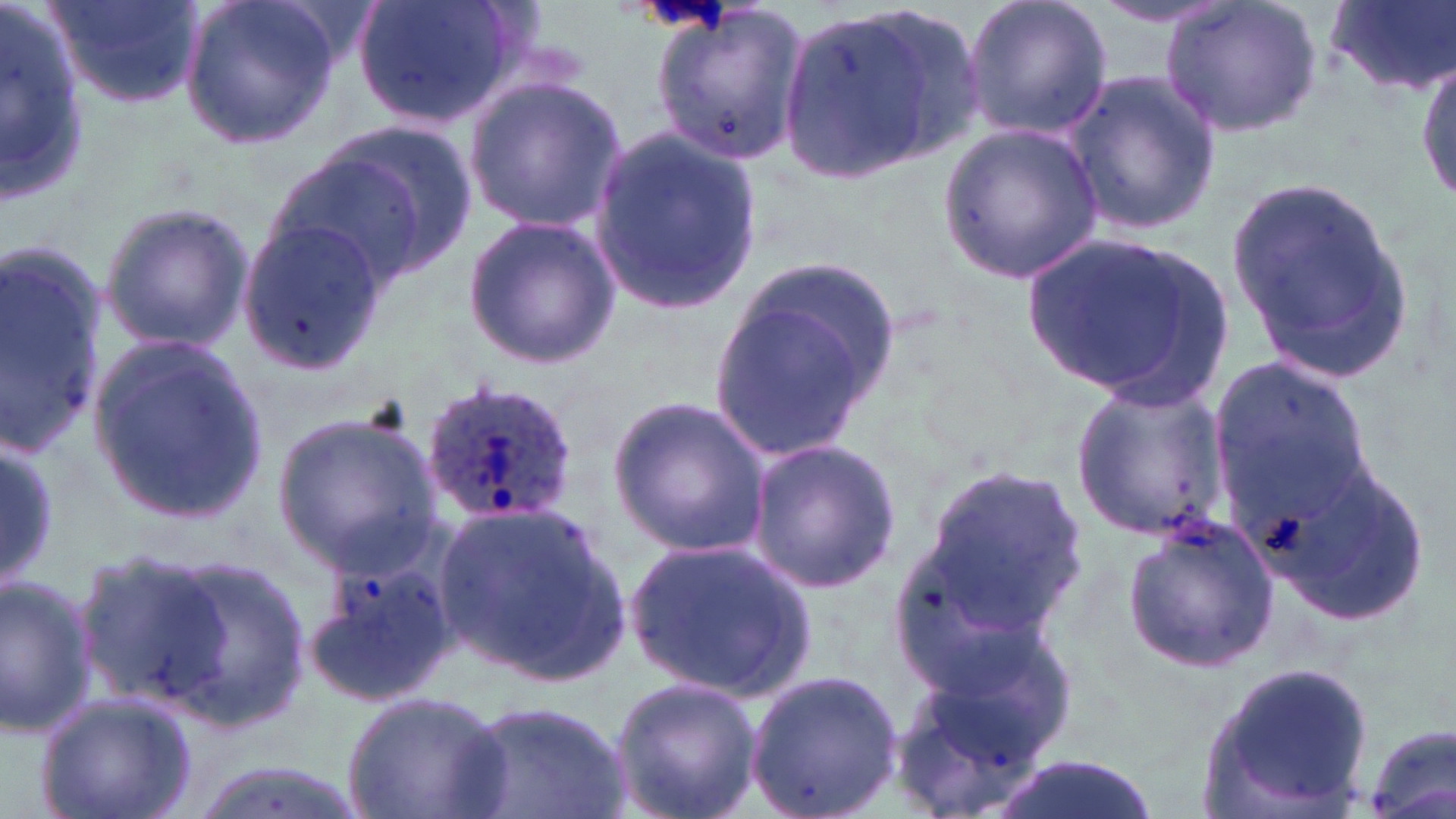
slide_level_diagnosis: Plasmodium ovale
magnification: 1000x
plasmodium_ovale_infected_red_blood_cell_locations: 'approximate bounding boxes as (x1, y1, x2, y2) in pixels: (420, 375, 582, 527)'
uninfected_red_blood_cell_locations: 'approximate bounding boxes as (x1, y1, x2, y2) in pixels: (0, 0, 96, 213), (48, 0, 206, 108), (178, 0, 342, 153), (352, 0, 523, 131), (961, 0, 1112, 142), (1159, 0, 1323, 139), (1322, 0, 1456, 97), (647, 1, 811, 163), (1089, 1, 1238, 27), (774, 14, 927, 185), (1415, 51, 1455, 213), (1059, 67, 1220, 237), (462, 75, 628, 233), (940, 123, 1103, 284), (271, 126, 476, 290), (589, 128, 765, 313), (1229, 177, 1418, 385), (97, 200, 254, 354), (461, 214, 621, 369), (236, 215, 392, 374), (1017, 231, 1233, 406), (0, 240, 111, 457), (702, 260, 900, 466), (84, 329, 265, 525), (1209, 353, 1374, 526), (1068, 380, 1230, 540), (609, 395, 771, 562), (271, 410, 443, 570), (744, 438, 902, 593), (0, 443, 60, 588), (1259, 458, 1429, 629), (917, 465, 1088, 637), (433, 500, 629, 683), (1119, 517, 1280, 677), (622, 536, 815, 699), (888, 546, 1049, 704), (69, 548, 247, 715), (304, 556, 456, 710), (143, 557, 311, 726), (0, 573, 98, 738), (884, 648, 1073, 816), (1194, 663, 1379, 819), (744, 671, 904, 818), (606, 675, 761, 819), (339, 688, 514, 819), (35, 690, 199, 819), (460, 698, 632, 819), (1360, 725, 1456, 819), (987, 754, 1160, 819), (182, 759, 369, 819)'
image_size: 1456×819 pixels
modality: optical microscopy
stain: May-Grünwald-Giemsa
field_of_view: single
preparation: thin blood film